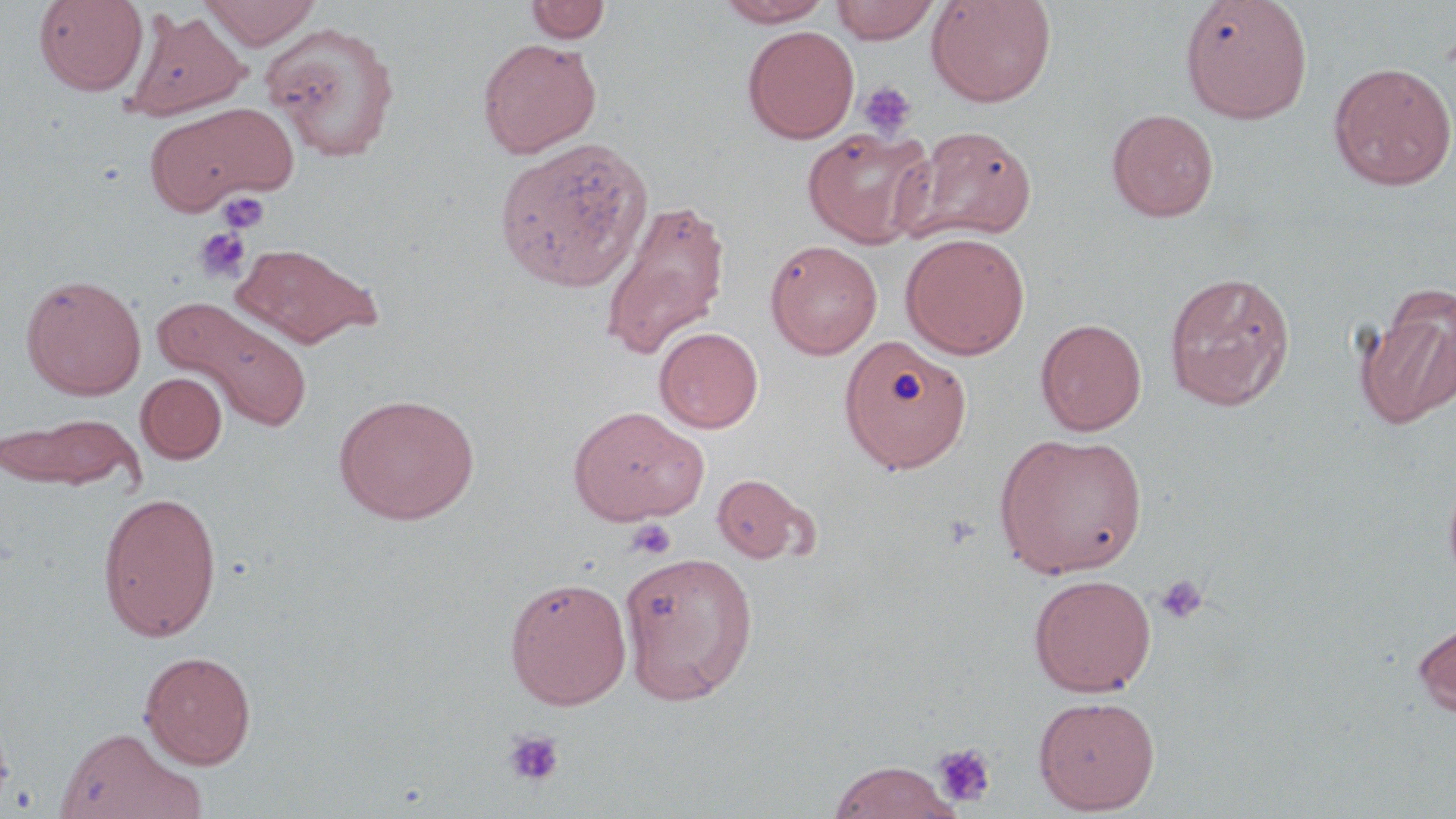
slide-level diagnosis = no evidence of blood parasites
stain = May-Grünwald-Giemsa
image size = 1456×819 pixels
magnification = 1000x
preparation = thin blood film
uninfected red blood cell locations = approximate bounding boxes as [x1, y1, x2, y2] in pixels: [34, 0, 148, 96], [200, 0, 321, 48], [714, 0, 834, 27], [926, 0, 1057, 108], [1180, 0, 1313, 123], [525, 1, 611, 44], [831, 1, 941, 43], [125, 7, 251, 121], [261, 22, 401, 162], [742, 25, 859, 144], [477, 37, 602, 158], [1327, 61, 1456, 190], [142, 100, 299, 215], [1105, 108, 1219, 222], [903, 125, 1037, 244], [802, 126, 935, 248], [494, 136, 654, 292], [599, 196, 731, 362], [900, 232, 1030, 359], [765, 239, 882, 358], [232, 240, 384, 348], [1164, 270, 1295, 410], [20, 274, 146, 400], [1359, 288, 1456, 429], [155, 296, 312, 432], [1035, 318, 1147, 436], [654, 326, 763, 433], [839, 335, 972, 473], [136, 372, 227, 463], [333, 393, 481, 525], [567, 405, 708, 526], [1, 410, 143, 493], [994, 432, 1148, 578], [712, 472, 811, 564], [97, 490, 223, 642], [620, 550, 759, 704], [1028, 573, 1156, 697], [504, 575, 632, 710], [1412, 615, 1456, 717], [139, 650, 257, 768], [1033, 695, 1160, 814], [54, 727, 206, 818], [825, 759, 963, 819]
modality = optical microscopy
platelet locations = approximate bounding boxes as [x1, y1, x2, y2] in pixels: [857, 81, 916, 139], [217, 191, 270, 234], [193, 227, 251, 284], [626, 518, 677, 560], [1153, 573, 1210, 626], [502, 730, 564, 788], [931, 744, 997, 809]
field of view = single